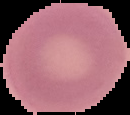
result: no Plasmodium parasites detected
image_type: segmented cell region with the area outside set to black
preparation: thin blood smear
image_size: 130×115 pixels